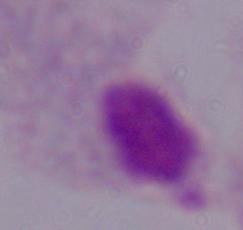 1000x magnification. A trichomonad is seen. Micrograph.